Name the parasite shown.
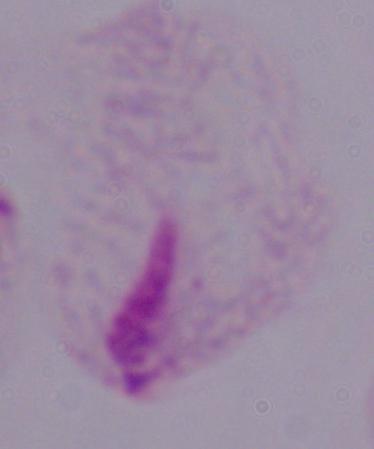

A trichomonad.

{
  "modality": "photomicrograph",
  "magnification": "1000x"
}